Classify this cell by malaria status.
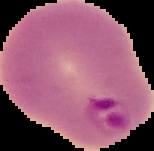
Parasitized.

preparation = thin blood smear
image size = 154×151 pixels
image type = segmented cell region on a black background